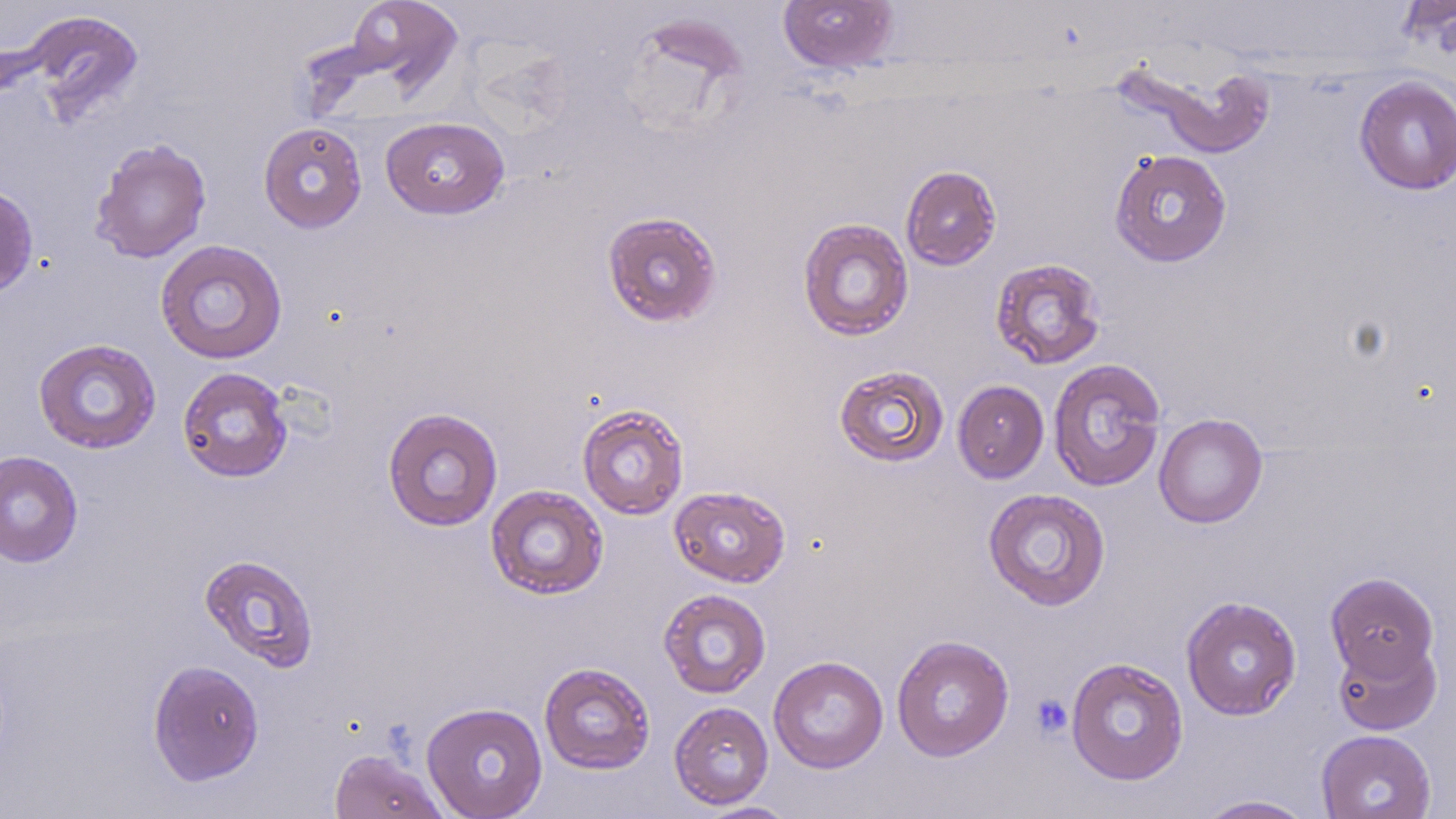
Approximate bounding boxes as (x1, y1, x2, y2) in pixels. Uninfected red blood cell locations: (345, 0, 463, 96), (777, 0, 899, 74), (24, 10, 145, 125), (1130, 61, 1277, 158), (1354, 75, 1456, 195), (380, 116, 509, 219), (258, 121, 368, 233), (90, 137, 212, 264), (1109, 149, 1232, 267), (900, 165, 1002, 271), (0, 184, 38, 298), (602, 209, 723, 327), (797, 217, 914, 341), (155, 239, 288, 365), (989, 258, 1107, 370), (32, 338, 162, 454), (1048, 358, 1166, 493), (833, 364, 950, 468), (177, 366, 293, 483), (952, 380, 1049, 483), (577, 403, 690, 520), (382, 406, 504, 532), (1154, 413, 1268, 528), (0, 450, 83, 568), (485, 485, 608, 600), (669, 485, 791, 587), (982, 487, 1111, 611), (198, 553, 320, 672), (1325, 571, 1439, 682), (658, 588, 771, 698), (1181, 595, 1302, 720), (890, 634, 1015, 762), (1332, 636, 1441, 735), (768, 655, 889, 774), (1065, 657, 1188, 786), (147, 660, 265, 786), (539, 662, 656, 775), (422, 701, 548, 819), (669, 701, 774, 809), (1316, 729, 1436, 819), (328, 748, 450, 819), (1196, 794, 1317, 818), (693, 801, 800, 818). Platelet locations: (1030, 694, 1073, 739). Slide-level diagnosis: negative for blood parasites. Single field of view. Optical microscopy. 1000x magnification. May-Grünwald-Giemsa-stained preparation. Thin blood smear. Image is 1456×819 pixels.